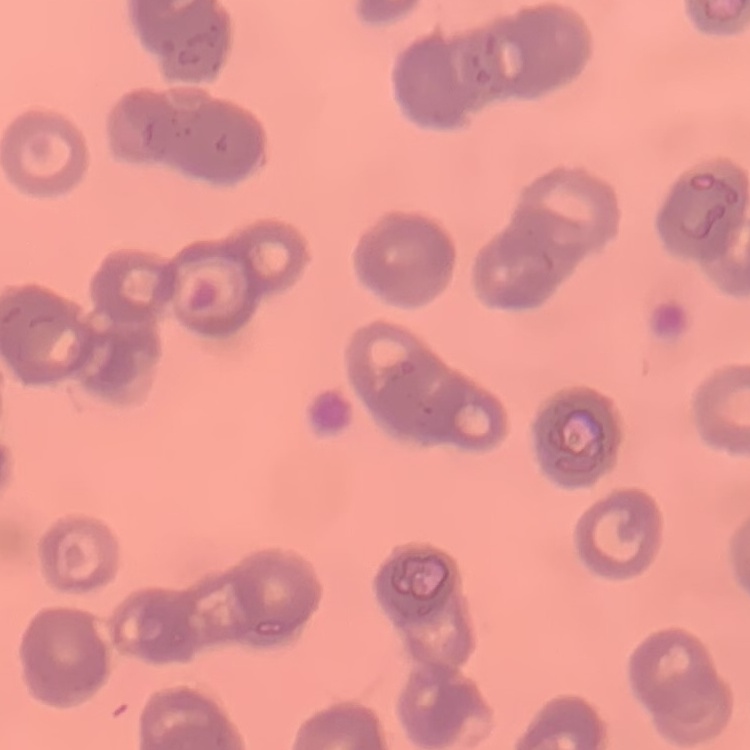 The red blood cells show rouleaux formation. Field's or Giemsa stain. Thin peripheral smear. Square crop of a larger photomicrograph.